Name the blood parasite species.
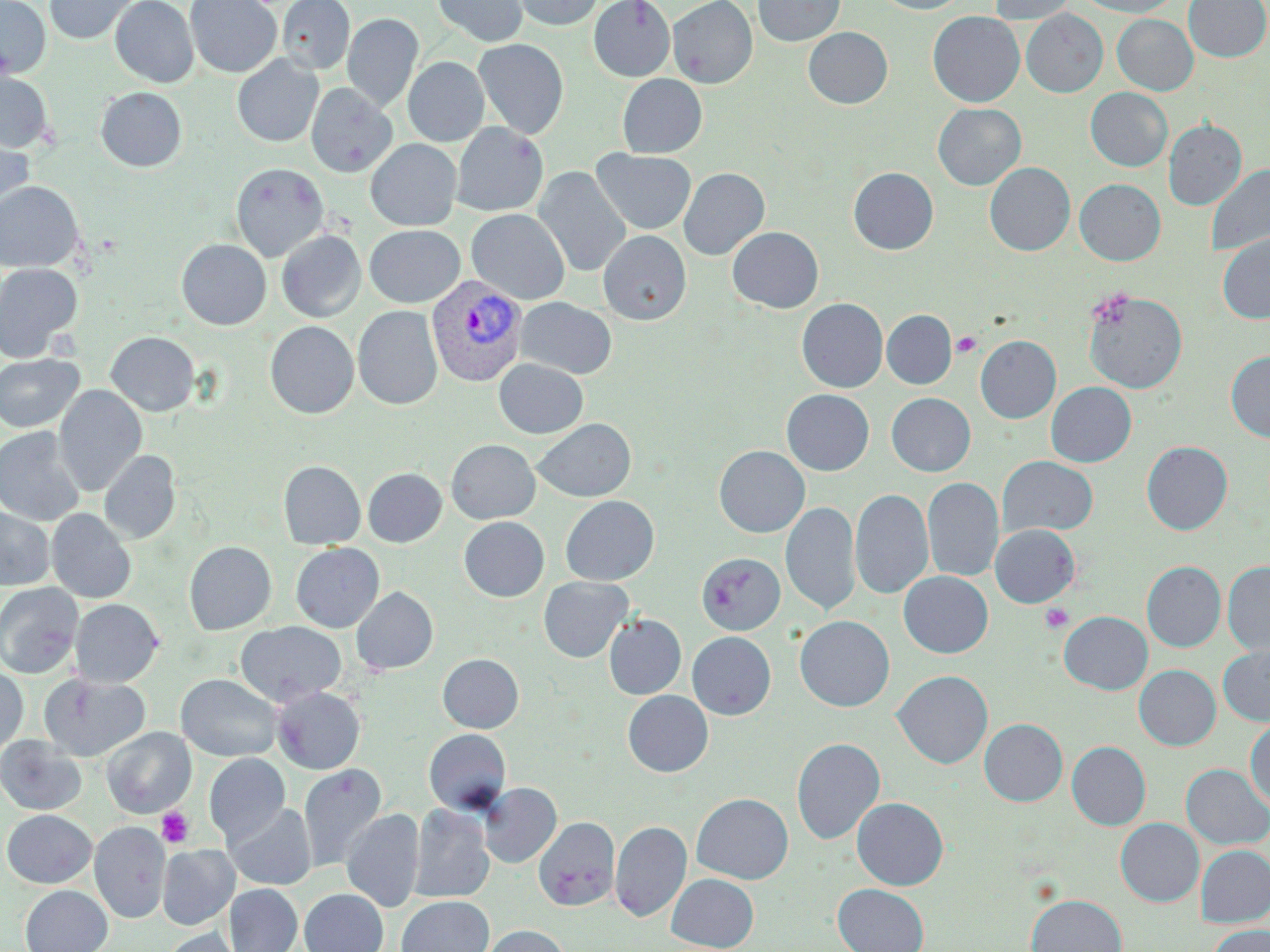

Plasmodium vivax.

Summary:
  - Coordinate format: approximate bounding boxes as (x1,y1)-(x2,y2) corner pairs in pixels
  - Uninfected red blood cell locations: (0,0)-(50,78), (44,0)-(139,44), (110,0)-(199,88), (185,0)-(282,77), (277,0)-(355,73), (433,0)-(528,47), (512,0)-(604,30), (589,0)-(675,81), (668,0)-(757,88), (753,0)-(845,45), (873,0)-(967,14), (988,0)-(1079,24), (1075,0)-(1180,17), (1184,0)-(1269,62), (1021,10)-(1108,97), (928,11)-(1025,107), (342,13)-(423,112), (1112,14)-(1198,95), (803,27)-(892,108), (473,38)-(569,139), (232,54)-(323,147), (403,57)-(489,146), (0,70)-(54,152), (617,74)-(707,157), (306,83)-(397,178), (95,87)-(187,172), (1085,88)-(1173,171), (933,103)-(1026,190), (1163,120)-(1246,210), (452,122)-(548,216), (0,132)-(34,220), (365,139)-(461,231), (592,149)-(696,234), (231,162)-(329,262), (985,162)-(1075,256), (1206,163)-(1270,258), (533,166)-(631,278), (848,167)-(939,254), (678,168)-(769,260), (1075,179)-(1165,266), (0,181)-(85,272), (466,209)-(569,304), (364,225)-(465,307), (727,226)-(823,312), (276,230)-(366,322), (598,230)-(691,325), (1218,234)-(1270,324), (177,238)-(271,330), (0,262)-(83,362), (1083,289)-(1188,394), (515,297)-(617,379), (797,298)-(888,392), (353,305)-(443,410), (882,310)-(956,389), (265,321)-(359,418), (106,331)-(200,416), (975,335)-(1061,423), (1226,350)-(1270,443), (0,353)-(84,432), (493,359)-(589,438), (1046,382)-(1136,467), (53,385)-(147,496), (782,389)-(874,475), (886,393)-(975,476), (533,418)-(636,501), (0,427)-(86,526), (446,439)-(540,523), (1142,441)-(1232,535), (714,445)-(810,537), (99,450)-(181,543), (997,456)-(1098,537), (278,460)-(366,549), (363,468)-(447,547), (922,477)-(1003,582), (850,488)-(934,600), (560,495)-(659,585), (781,501)-(860,617), (0,507)-(55,590), (46,509)-(136,603), (458,517)-(549,601), (990,524)-(1080,607), (184,541)-(277,635), (290,543)-(384,632), (696,553)-(785,635), (1141,560)-(1226,652), (1222,561)-(1270,656), (899,571)-(993,658), (538,576)-(634,662), (0,582)-(83,678), (352,586)-(438,675), (70,598)-(164,687), (1059,611)-(1152,694), (604,614)-(686,699), (795,615)-(894,711), (236,621)-(346,706), (687,632)-(776,720), (1218,643)-(1270,727), (438,653)-(524,732), (0,665)-(28,757), (1134,665)-(1221,750), (892,670)-(993,769), (39,673)-(150,760), (176,674)-(283,761), (273,687)-(365,774), (623,690)-(713,776), (1246,716)-(1270,810), (979,718)-(1068,806), (102,727)-(195,818), (423,729)-(512,814), (1,735)-(87,815), (791,737)-(885,844), (1066,741)-(1150,830), (204,754)-(289,845), (1181,764)-(1269,849), (298,765)-(386,873), (479,783)-(562,868), (691,793)-(793,884), (851,797)-(948,890), (225,802)-(316,890), (409,804)-(495,903), (341,808)-(424,912), (2,809)-(96,888), (533,816)-(620,912), (1116,818)-(1204,906), (610,820)-(692,922), (90,822)-(170,923), (157,844)-(239,929), (1196,845)-(1270,926), (666,873)-(759,951), (833,883)-(929,952), (225,884)-(302,952), (20,885)-(112,952), (299,888)-(388,952), (1026,894)-(1127,952), (396,896)-(493,952), (483,925)-(570,952), (1207,925)-(1270,952), (162,927)-(244,952)
  - Platelet locations: (952,332)-(982,357), (1040,603)-(1073,633), (156,807)-(193,848)
  - Plasmodium vivax-infected red blood cell locations: (426,274)-(528,387)
  - Modality: light microscopy
  - Stain: May-Grünwald-Giemsa
  - Image size: 1270×952 pixels
  - Field of view: one of a larger specimen
  - Preparation: thin blood smear
  - Magnification: 1000x